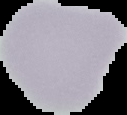
malaria status = uninfected
image size = 127×115 pixels
preparation = thin blood film
image type = cell region segmented out of the field of view; surrounding area masked to black